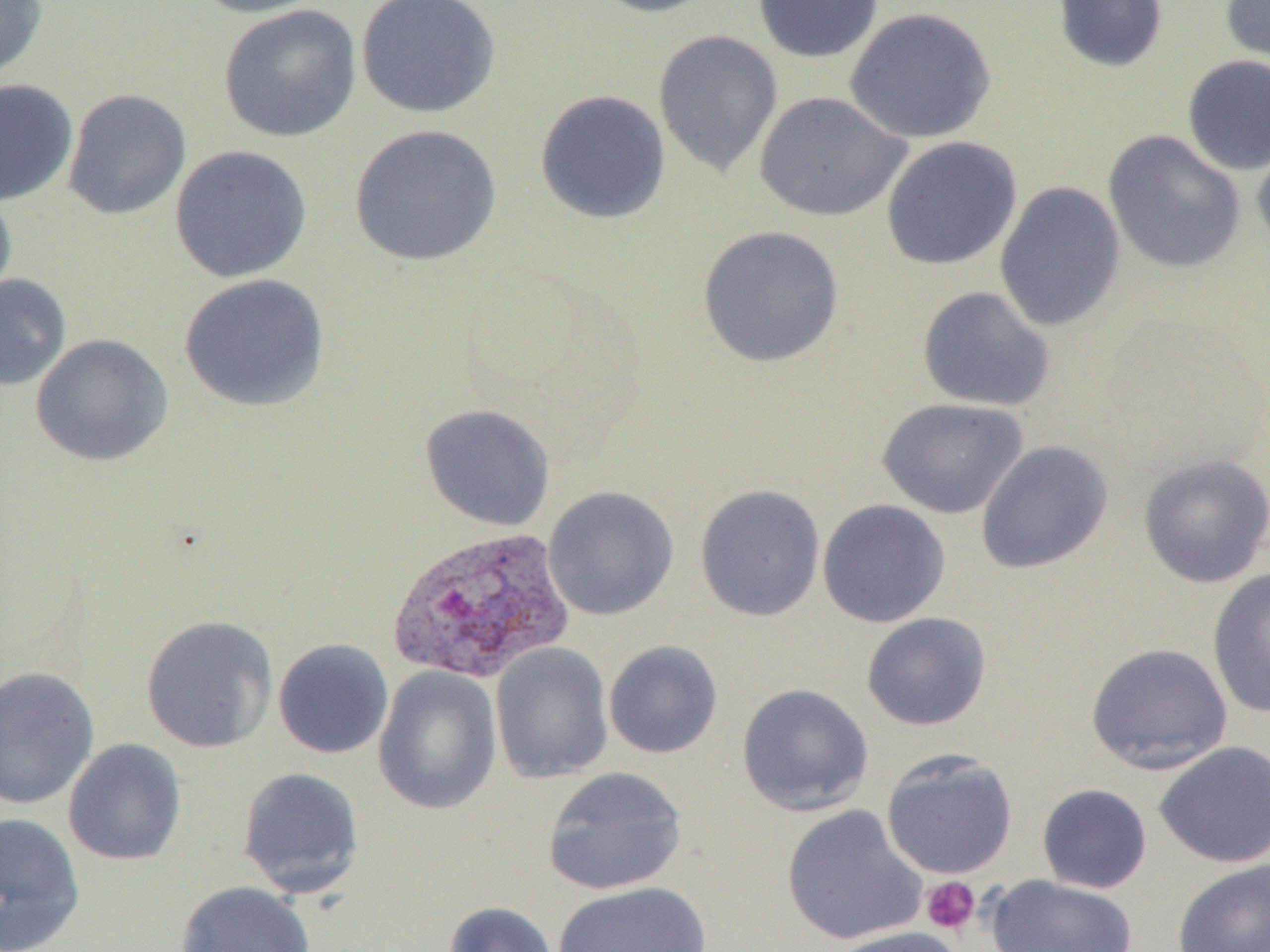
Summary:
  - Coordinate format: approximate bounding boxes as (x1, y1, x2, y2) in pixels
  - Plasmodium vivax-infected red blood cell locations: (386, 526, 576, 684)
  - Uninfected red blood cell locations: (0, 0, 48, 83), (185, 0, 332, 19), (356, 0, 501, 119), (585, 0, 719, 18), (752, 0, 883, 63), (1052, 0, 1168, 73), (1220, 0, 1270, 78), (218, 4, 362, 143), (844, 7, 996, 144), (653, 29, 783, 177), (1181, 54, 1269, 175), (0, 79, 79, 206), (63, 88, 192, 220), (534, 89, 672, 224), (754, 91, 912, 222), (348, 124, 503, 267), (1252, 129, 1270, 260), (1102, 130, 1246, 274), (881, 136, 1022, 270), (169, 145, 313, 283), (994, 181, 1126, 333), (0, 186, 17, 310), (697, 225, 844, 368), (178, 273, 330, 412), (0, 274, 71, 390), (917, 285, 1056, 412), (30, 333, 173, 467), (876, 397, 1029, 519), (420, 403, 555, 531), (975, 440, 1114, 575), (1136, 452, 1270, 588), (694, 483, 826, 621), (542, 486, 679, 621), (817, 499, 951, 628), (1206, 567, 1270, 719), (861, 612, 992, 731), (140, 615, 278, 754), (273, 638, 394, 759), (603, 640, 723, 759), (1084, 642, 1234, 774), (490, 643, 614, 783), (0, 666, 100, 810), (373, 666, 502, 815), (736, 683, 874, 816), (63, 738, 187, 866), (1153, 741, 1270, 868), (880, 750, 1019, 879), (236, 766, 365, 898), (541, 766, 687, 896), (1037, 784, 1153, 894), (780, 804, 927, 947), (0, 812, 86, 951), (1172, 859, 1270, 952), (986, 875, 1139, 952), (175, 881, 316, 952), (552, 881, 711, 951), (444, 901, 560, 952), (827, 926, 969, 952)
  - Platelet locations: (921, 876, 980, 935)
  - Slide-level diagnosis: Plasmodium vivax
  - Modality: light microscopy
  - Image size: 1270×952 pixels
  - Field of view: single
  - Preparation: thin blood smear
  - Magnification: 1000x